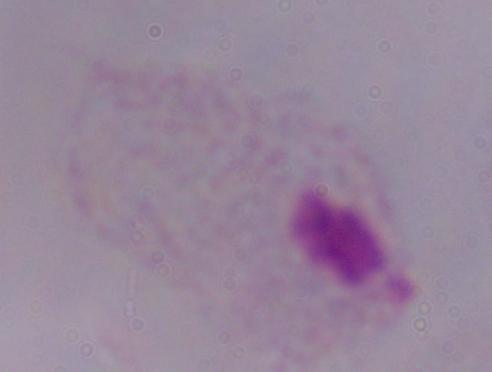
Summary:
  - Modality: micrograph
  - Magnification: 1000x
  - Identification: trichomonad